Locate and identify every blood parasite.
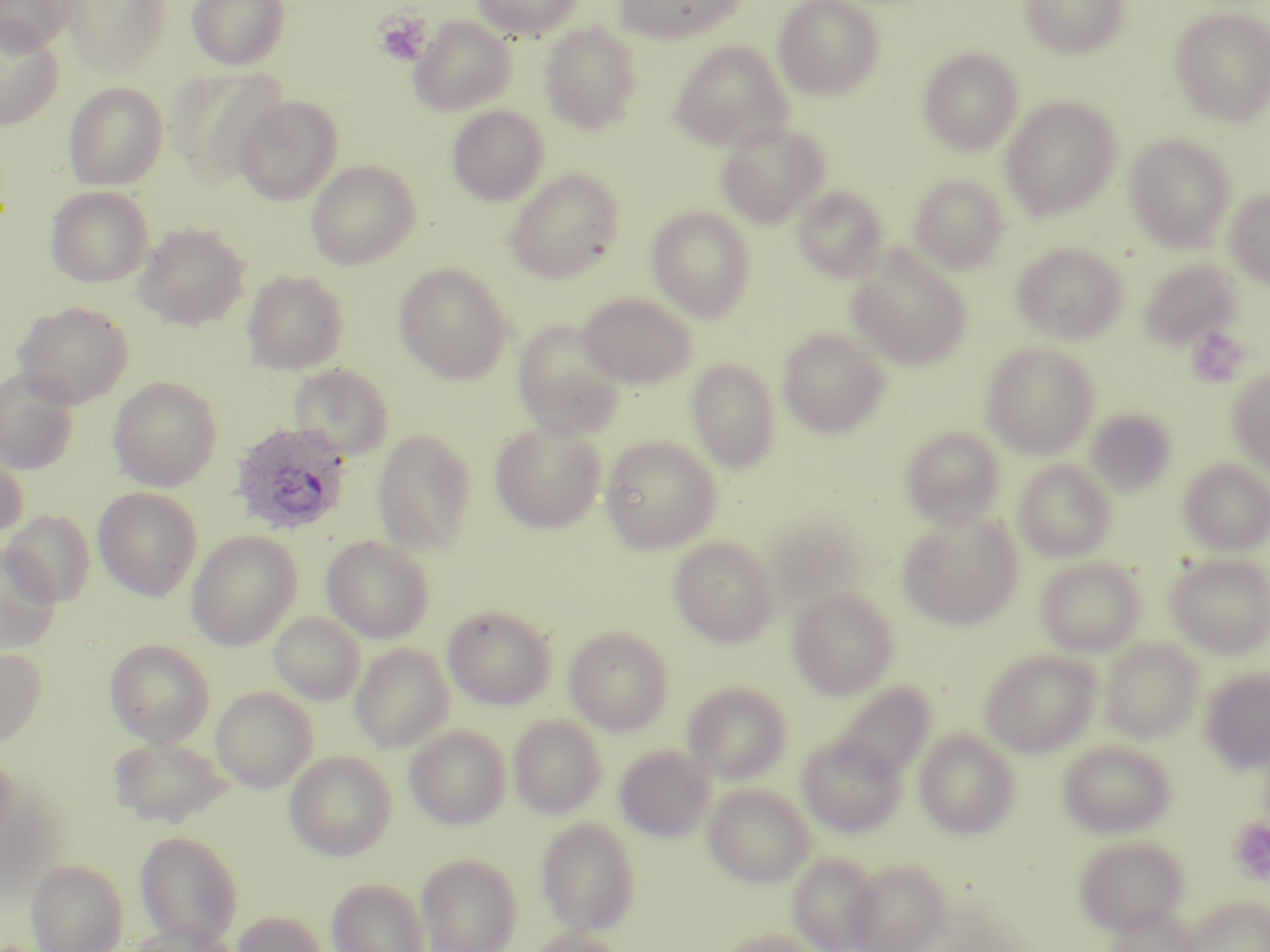

Approximate bounding boxes as (x1, y1, x2, y2) in pixels.
Plasmodium ovale-infected red blood cells: (230, 422, 352, 536).
No Plasmodium falciparum, Plasmodium malariae, Plasmodium vivax, Babesia divergens, or Trypanosoma brucei observed.

Summary:
  - Uninfected red blood cell locations (subset): (62, 0, 172, 80), (188, 0, 291, 70), (471, 0, 583, 40), (614, 0, 747, 44), (773, 0, 885, 100), (1020, 0, 1129, 59), (0, 1, 75, 51), (1169, 5, 1270, 128), (409, 16, 517, 116), (0, 19, 64, 128), (539, 21, 644, 135), (668, 41, 793, 152), (917, 46, 1024, 156), (167, 67, 286, 188), (63, 82, 169, 190), (233, 94, 343, 205), (1000, 96, 1121, 220), (446, 104, 549, 206), (715, 121, 830, 228), (1125, 133, 1236, 252), (306, 160, 420, 269), (504, 167, 626, 283), (908, 174, 1010, 273), (791, 185, 889, 281), (46, 186, 153, 288), (1224, 189, 1270, 287), (646, 205, 756, 322), (133, 222, 250, 330), (1010, 243, 1129, 344), (847, 248, 972, 370), (1137, 257, 1242, 350), (394, 262, 513, 385), (242, 269, 349, 375), (578, 293, 697, 389), (13, 300, 134, 409), (512, 319, 626, 439), (777, 327, 891, 439), (981, 341, 1100, 459), (686, 358, 781, 473), (286, 363, 394, 460), (0, 368, 79, 475), (1228, 368, 1270, 475), (108, 376, 222, 491), (1086, 407, 1177, 495), (490, 421, 607, 533), (901, 426, 1006, 530), (372, 428, 478, 556), (600, 435, 722, 554), (0, 447, 28, 544), (1178, 459, 1270, 555), (1013, 460, 1117, 561), (93, 487, 203, 600), (3, 510, 96, 606), (763, 514, 871, 613), (896, 514, 1022, 629), (186, 531, 302, 650), (321, 535, 435, 643), (669, 536, 778, 647), (0, 544, 61, 656), (1164, 553, 1270, 658), (1035, 557, 1145, 656), (787, 587, 899, 700), (443, 604, 557, 710), (269, 611, 366, 705), (564, 627, 673, 734), (105, 639, 215, 747), (1100, 639, 1206, 742), (350, 643, 455, 753), (0, 648, 46, 749), (979, 650, 1101, 758), (1200, 668, 1270, 771), (697, 680, 800, 885), (682, 681, 793, 784), (833, 681, 936, 781), (211, 686, 317, 792), (508, 715, 607, 818), (405, 725, 511, 830), (914, 728, 1020, 839), (797, 734, 906, 837), (109, 736, 231, 827), (1057, 740, 1177, 838), (614, 745, 714, 841), (0, 749, 17, 853), (285, 750, 396, 861), (703, 784, 814, 887), (536, 818, 640, 935), (135, 830, 244, 948), (1073, 836, 1189, 935), (416, 853, 522, 952), (787, 853, 884, 952), (845, 859, 951, 952), (27, 860, 128, 952), (327, 878, 430, 952), (1185, 895, 1270, 952), (1104, 905, 1201, 952), (231, 910, 329, 952), (126, 923, 241, 952), (715, 928, 826, 952), (527, 929, 629, 952)
  - Platelet locations (subset): (373, 11, 432, 66), (1188, 326, 1250, 386)
  - Slide-level diagnosis: Plasmodium ovale
  - Magnification: 1000x
  - Preparation: thin blood smear
  - Stain: May-Grünwald-Giemsa
  - Modality: optical microscopy
  - Image size: 1270×952 pixels
  - Field of view: single